Give the extent of all Plasmodium falciparum-infected red blood cells.
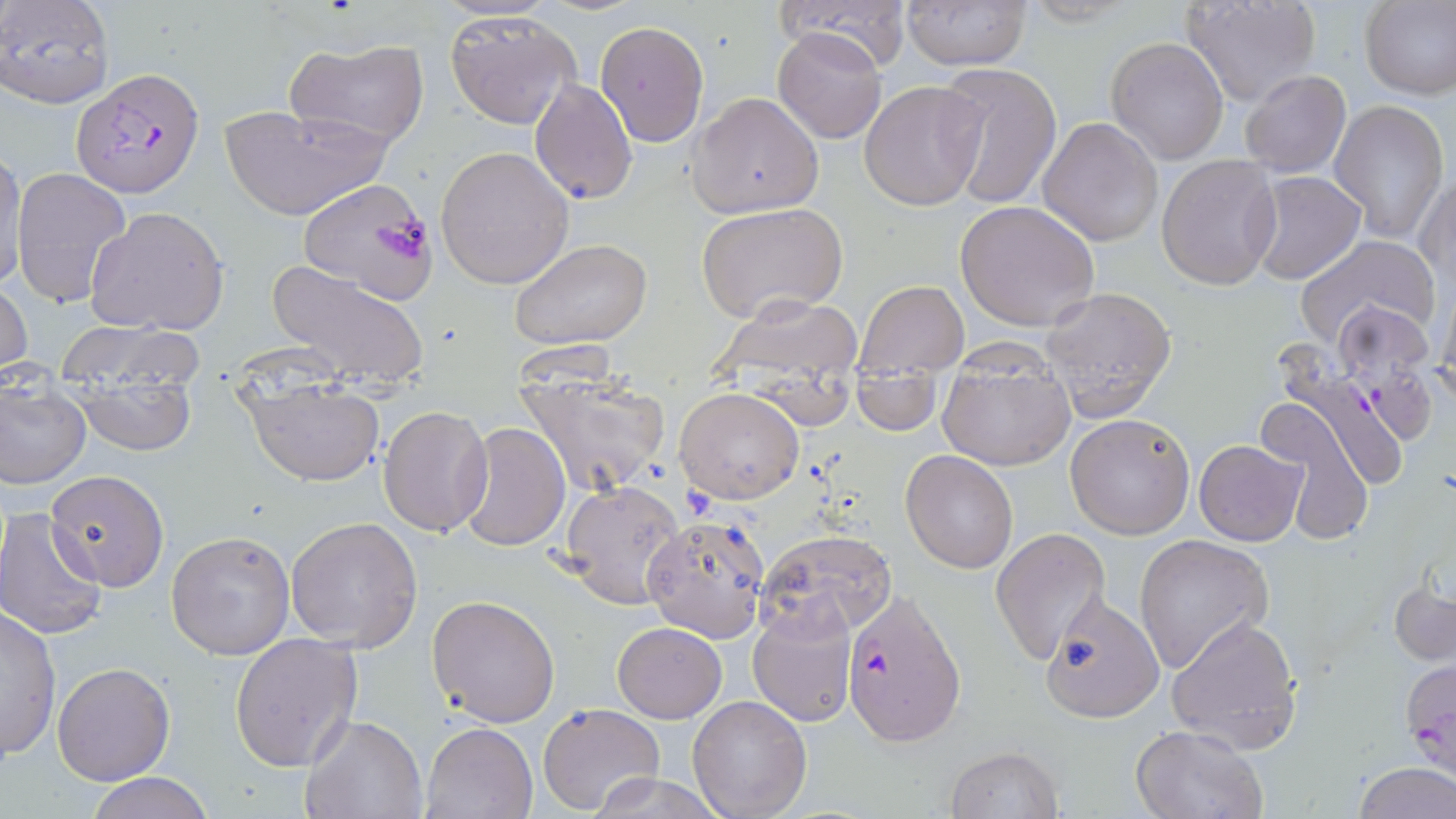
Approximate bounding boxes as (x1,y1)-(x2,y2) corner pairs in pixels.
Plasmodium falciparum-infected red blood cells: (70,67)-(205,196), (1270,339)-(1408,494), (840,590)-(966,746).

Uninfected red blood cell locations: (0,0)-(114,108), (776,0)-(914,72), (1182,0)-(1324,108), (899,1)-(1033,71), (1360,1)-(1456,101), (445,10)-(581,129), (594,20)-(711,148), (773,27)-(887,144), (286,37)-(431,149), (1106,37)-(1229,164), (936,60)-(1062,210), (1237,70)-(1351,178), (530,77)-(638,205), (859,80)-(988,212), (688,92)-(824,219), (1330,100)-(1449,245), (218,102)-(391,222), (1037,116)-(1164,248), (435,145)-(574,289), (1,147)-(29,291), (1156,153)-(1283,291), (11,166)-(133,308), (1245,171)-(1365,286), (1416,171)-(1455,287), (298,179)-(438,303), (955,200)-(1100,332), (695,202)-(848,325), (84,206)-(229,337), (1295,234)-(1441,354), (510,239)-(652,351), (266,258)-(431,393), (0,278)-(33,382), (856,280)-(969,376), (1042,287)-(1176,420), (1435,288)-(1456,406), (702,292)-(871,417), (59,323)-(206,455), (938,349)-(1076,473), (513,361)-(671,498), (853,370)-(941,435), (242,372)-(385,488), (0,376)-(91,490), (675,388)-(804,504), (1258,399)-(1373,546), (377,404)-(492,538), (1065,412)-(1195,540), (459,421)-(570,552), (1193,439)-(1306,546), (902,450)-(1017,574), (46,471)-(170,592), (557,477)-(687,608), (0,511)-(108,640), (641,514)-(771,642), (286,516)-(424,653), (990,528)-(1111,667), (759,529)-(896,638), (166,530)-(294,660), (1134,534)-(1274,674), (1389,576)-(1456,668), (427,594)-(561,726), (1040,596)-(1165,722), (747,601)-(857,729), (1,607)-(62,760), (1166,615)-(1303,753), (612,621)-(726,722), (228,632)-(363,774), (52,663)-(174,785), (687,695)-(812,819), (537,703)-(665,816), (299,714)-(428,819), (421,720)-(539,818), (1130,725)-(1266,819), (945,747)-(1063,819), (1353,764)-(1455,819), (587,770)-(727,819), (83,773)-(217,818). Slide-level diagnosis: Plasmodium falciparum. One field of a larger specimen. Light microscopy. Thin blood film. 1000x magnification. May-Grünwald-Giemsa-stained preparation. Image is 1456×819 pixels.